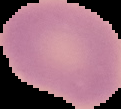

{
  "image_type": "segmented cell region on a black background",
  "image_size": "121×109 pixels",
  "preparation": "thin blood film",
  "malaria_status": "uninfected"
}